Report the malaria status of this cell.
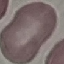
Uninfected.

capture: smartphone camera at the microscope eyepiece
preparation: thin blood film
stain: Giemsa
image_type: cell patch, automatically extracted from a larger field of view and resized to 64 × 64 pixels